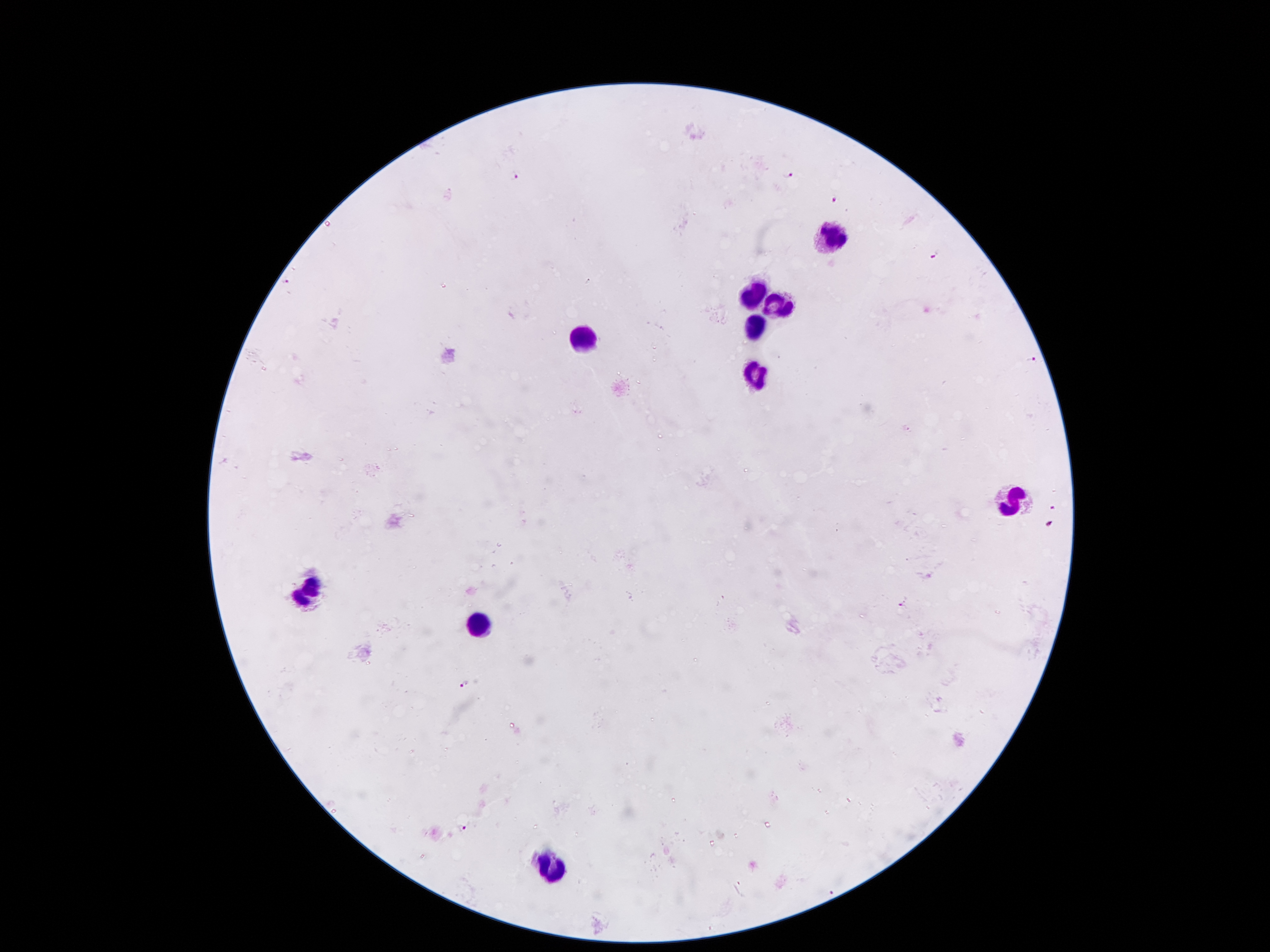
coordinate format = approximate object centers, in pixels from the top-left corner
Plasmodium parasite locations = (x=517, y=175), (x=786, y=175), (x=836, y=197), (x=937, y=255), (x=288, y=279), (x=1034, y=359), (x=1051, y=506), (x=1050, y=523), (x=926, y=575), (x=900, y=604), (x=463, y=685), (x=463, y=829), (x=830, y=892)
leukocyte locations = (x=831, y=241), (x=754, y=294), (x=781, y=304), (x=758, y=329), (x=581, y=339), (x=758, y=372), (x=1011, y=502), (x=307, y=590), (x=477, y=626), (x=556, y=866)
magnification = 100x
image size = 1270×952 pixels
preparation = thick peripheral-blood smear
stain = Giemsa
capture = smartphone through the microscope eyepiece
field of view = one from this slide
patient malaria status = infected with Plasmodium falciparum